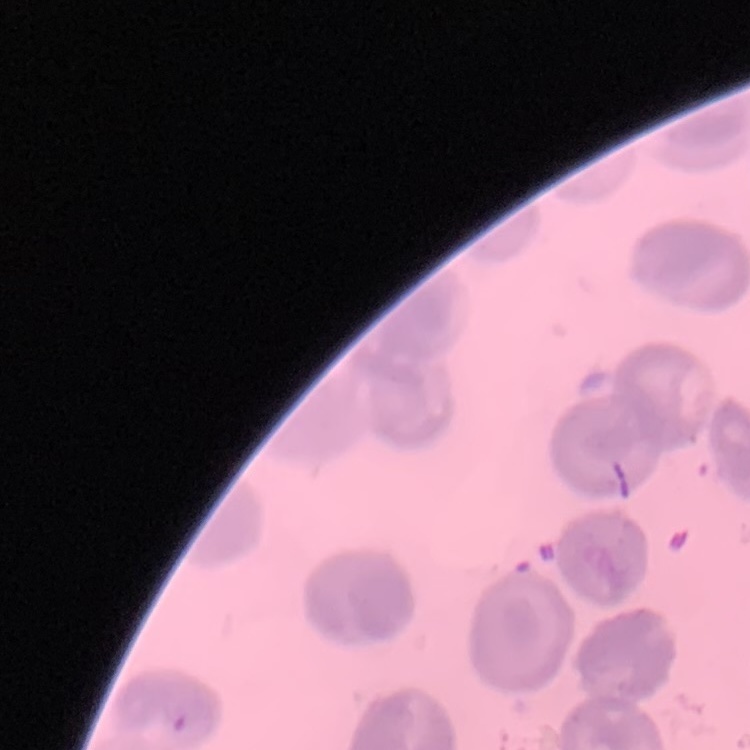

{
  "erythrocyte_morphology": "no rouleaux formation",
  "preparation": "thin blood smear",
  "stain": "Field's or Giemsa",
  "image_type": "one tile cut from a larger photomicrograph"
}